State the blood parasite species.
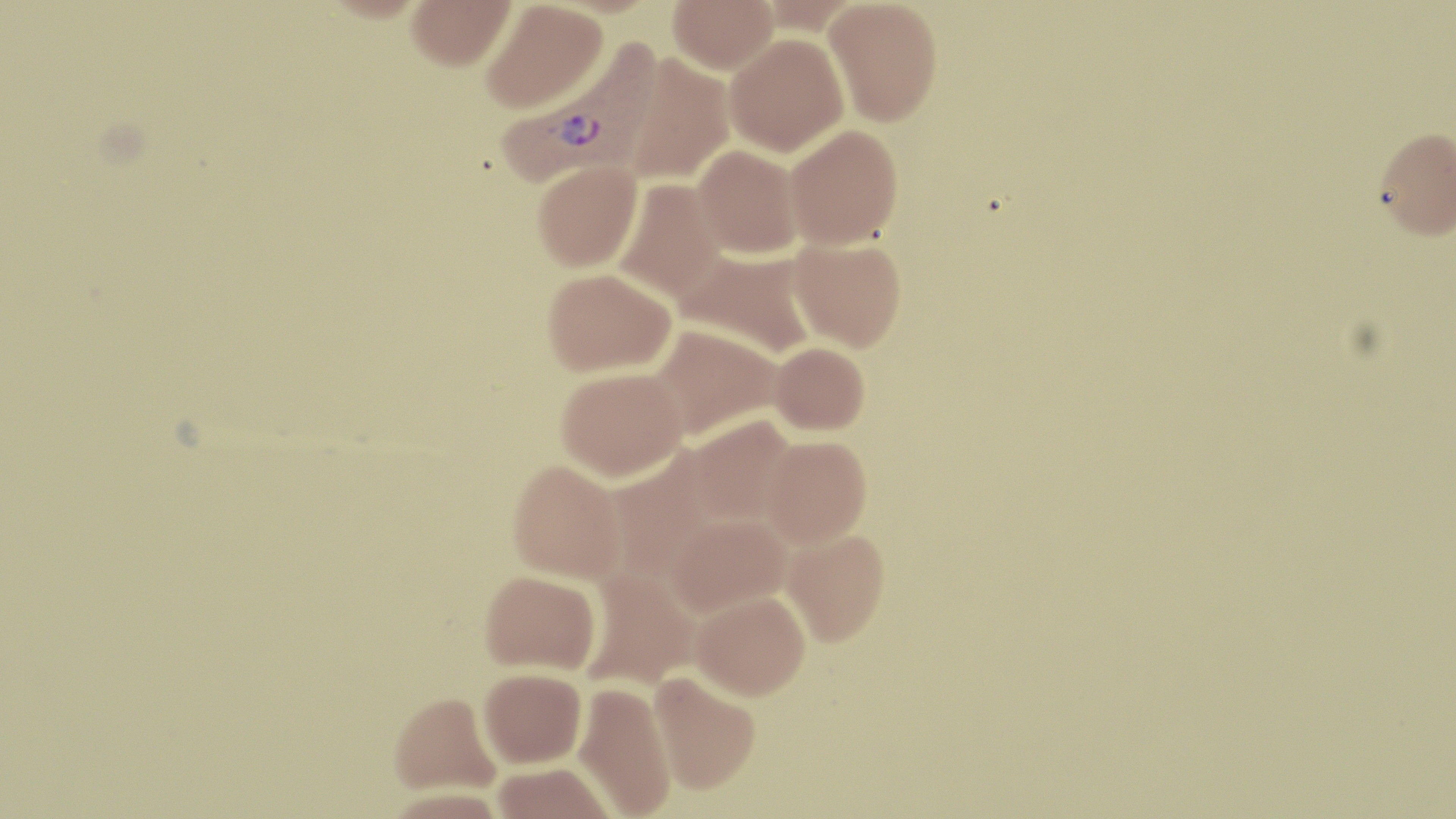

Plasmodium vivax.

Approximate bounding boxes as named x1/y1/x2/y2 corners in pixels. Plasmodium vivax-infected red blood cell locations: (x1=496, y1=38, x2=661, y2=186). Uninfected red blood cell locations: (x1=317, y1=0, x2=433, y2=22), (x1=406, y1=0, x2=516, y2=70), (x1=480, y1=0, x2=607, y2=113), (x1=668, y1=0, x2=778, y2=74), (x1=823, y1=1, x2=942, y2=126), (x1=723, y1=32, x2=849, y2=156), (x1=620, y1=53, x2=736, y2=185), (x1=785, y1=125, x2=903, y2=249), (x1=1374, y1=126, x2=1456, y2=240), (x1=693, y1=145, x2=802, y2=258), (x1=532, y1=160, x2=642, y2=271), (x1=612, y1=178, x2=726, y2=302), (x1=789, y1=238, x2=907, y2=352), (x1=675, y1=248, x2=818, y2=359), (x1=542, y1=267, x2=675, y2=376), (x1=647, y1=322, x2=782, y2=440), (x1=769, y1=341, x2=870, y2=435), (x1=556, y1=366, x2=687, y2=481), (x1=685, y1=415, x2=796, y2=527), (x1=761, y1=434, x2=871, y2=548), (x1=602, y1=448, x2=719, y2=582), (x1=507, y1=459, x2=626, y2=584), (x1=664, y1=513, x2=792, y2=618), (x1=781, y1=528, x2=890, y2=645), (x1=580, y1=568, x2=701, y2=691), (x1=480, y1=570, x2=600, y2=674), (x1=691, y1=589, x2=810, y2=699), (x1=479, y1=667, x2=587, y2=768), (x1=649, y1=670, x2=762, y2=795), (x1=574, y1=682, x2=677, y2=818), (x1=389, y1=691, x2=501, y2=795), (x1=491, y1=762, x2=616, y2=819). Thin blood smear. Optical microscopy. Image is 1456×819 pixels. 1000x magnification. May-Grünwald-Giemsa-stained preparation. Single field of view.